Mark where leukocytes are.
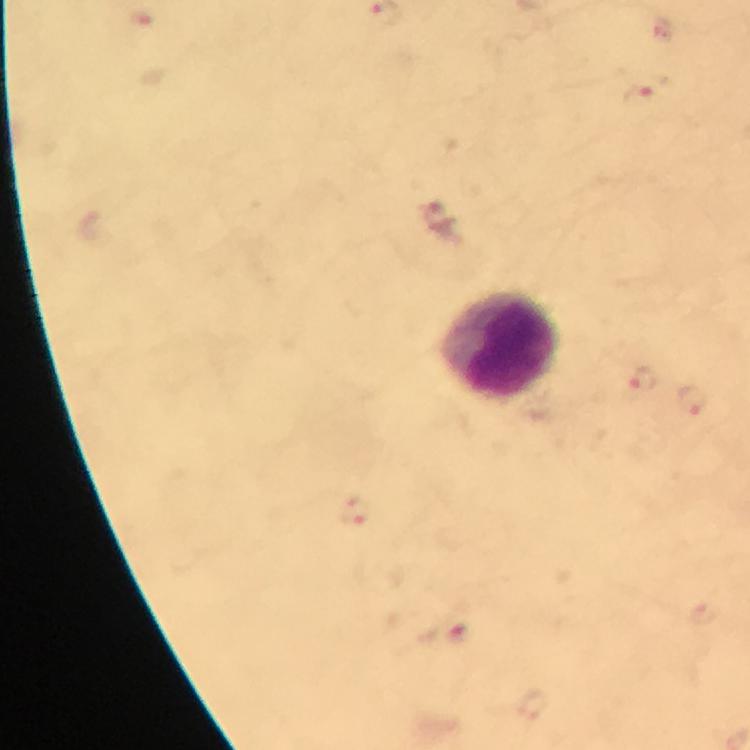
Approximate centers as {x, y} in pixels.
Leukocytes: {499, 344}.

capture = smartphone photograph through a microscope
context = from a diagnostic examination for malaria
magnification = 100x
cropped from = one field of view
image size = 750×750 pixels
preparation = thick blood film
stain = Giemsa
malaria parasite locations = approximate centers as {x, y} in pixels: {636, 94}, {643, 379}, {354, 511}
immersion oil = used